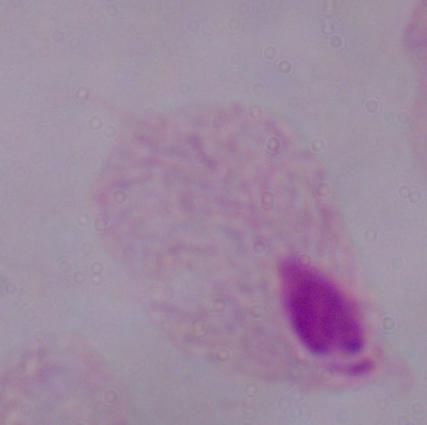
1000x magnification. Micrograph. A trichomonad is seen.